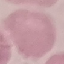
result = negative for malaria parasites
image type = cell patch, automatically extracted from a larger field of view and resized to 64 × 64 pixels
preparation = thin blood film
capture = smartphone through the microscope eyepiece
stain = Giemsa